Report the malaria status of this cell.
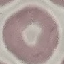

It is uninfected.

Giemsa stain. Acquired by smartphone through the microscope eyepiece. Automatically extracted cell patch, resized to 64 × 64 pixels. Thin blood film.